Give the extent of all uninfected red blood cells.
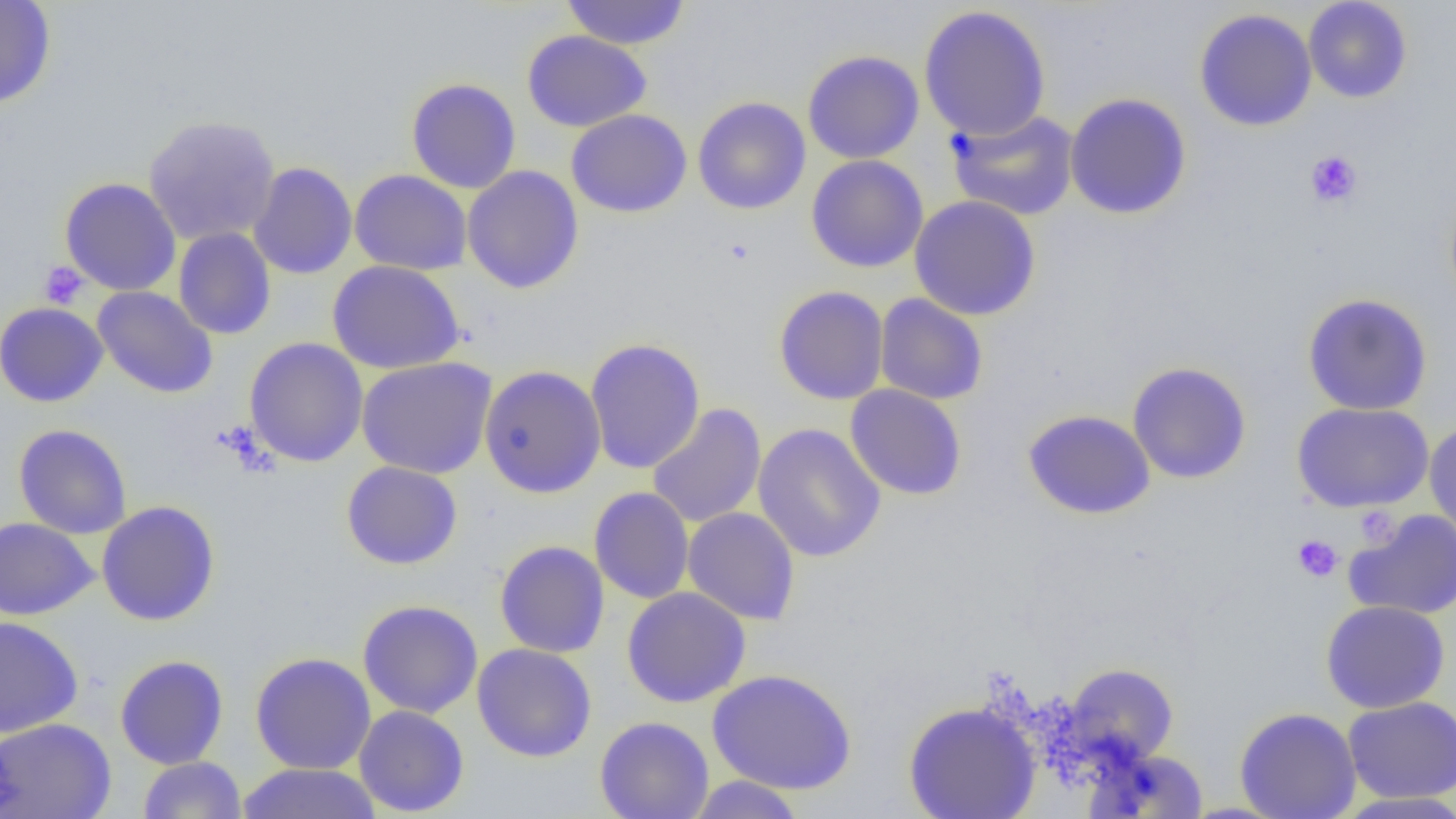
Approximate bounding boxes as (x1, y1, x2, y2) in pixels.
Uninfected red blood cells: (0, 0, 56, 109), (560, 0, 692, 50), (1303, 0, 1413, 103), (918, 5, 1051, 141), (1194, 8, 1317, 131), (522, 30, 651, 132), (802, 50, 924, 164), (406, 77, 521, 193), (1064, 92, 1192, 220), (692, 96, 811, 215), (566, 109, 692, 218), (945, 109, 1080, 221), (143, 114, 281, 246), (806, 155, 929, 273), (248, 161, 358, 279), (462, 165, 584, 294), (349, 169, 472, 276), (59, 177, 181, 296), (909, 195, 1041, 321), (173, 227, 276, 339), (327, 260, 465, 374), (92, 285, 218, 398), (773, 285, 889, 405), (1302, 293, 1433, 415), (874, 294, 988, 405), (0, 302, 108, 407), (244, 337, 368, 467), (585, 338, 705, 473), (356, 357, 497, 479), (1127, 362, 1252, 484), (479, 364, 606, 498), (845, 384, 967, 501), (1292, 402, 1434, 513), (647, 403, 766, 528), (1023, 409, 1155, 519), (1424, 421, 1456, 543), (752, 423, 887, 563), (14, 424, 132, 539), (341, 461, 463, 570), (589, 487, 694, 604), (96, 501, 220, 626), (682, 507, 800, 624), (1344, 509, 1456, 620), (0, 517, 97, 620), (494, 540, 610, 658), (622, 587, 751, 708), (357, 599, 483, 719), (1321, 600, 1450, 713), (0, 616, 83, 737), (472, 643, 597, 762), (250, 652, 376, 775), (115, 654, 229, 769), (1062, 662, 1179, 767), (707, 668, 857, 795), (1343, 695, 1456, 804), (903, 702, 1040, 819), (354, 705, 469, 817), (1234, 707, 1361, 819), (595, 716, 714, 819), (0, 717, 115, 819), (1090, 749, 1210, 817), (138, 756, 247, 818), (235, 763, 382, 818), (686, 775, 807, 819), (1334, 792, 1456, 818).

slide-level diagnosis = no evidence of blood parasites
platelet locations = approximate bounding boxes as (x1, y1, x2, y2) in pixels: (1305, 150, 1363, 209), (39, 261, 88, 308), (1354, 507, 1400, 547), (1292, 534, 1343, 582)
modality = optical microscopy
image size = 1456×819 pixels
preparation = thin blood smear
magnification = 1000x
field of view = single